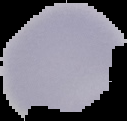 Malaria status: uninfected. From a thin blood smear. Image is 127×121 pixels. Segmented cell region on a black background.